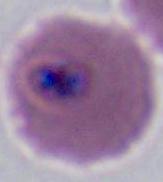
magnification = 400x or 1000x
identification = Plasmodium
modality = micrograph